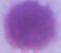

magnification = 1000x
identification = erythrocyte
modality = micrograph